Report the malaria status of this cell.
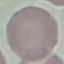
It is uninfected.

Summary:
  - Capture: smartphone through the microscope eyepiece
  - Preparation: thin blood film
  - Stain: Giemsa
  - Image type: cell patch, automatically extracted from a larger field of view and resized to 64 × 64 pixels